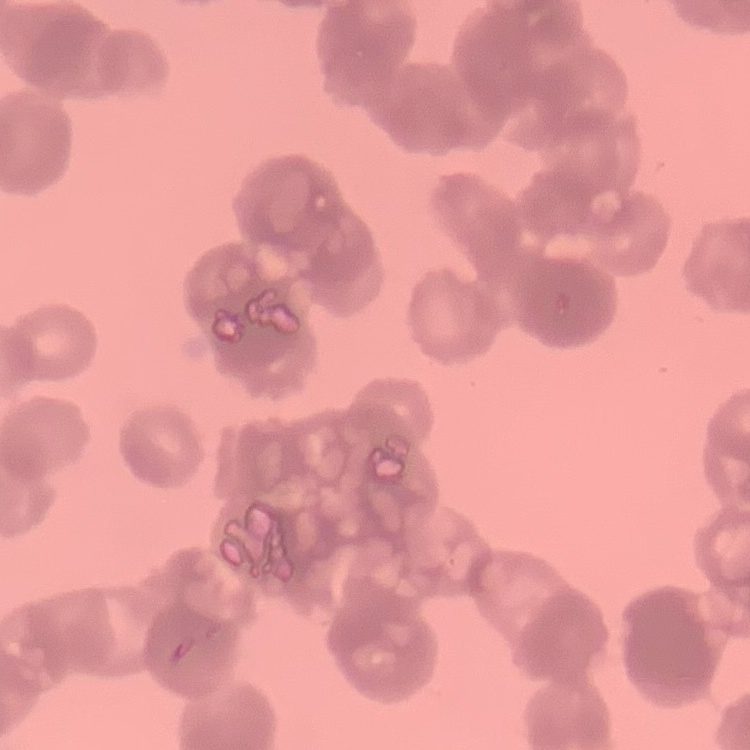
Summary:
  - Erythrocyte morphology: rouleaux formation
  - Preparation: thin blood film
  - Image type: one tile cut from a larger photomicrograph
  - Stain: Field's or Giemsa